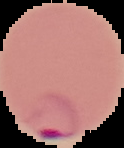

{
  "preparation": "thin blood film",
  "image_type": "segmented cell region on a black background",
  "image_size": "124×148 pixels",
  "malaria_status": "parasitized"
}